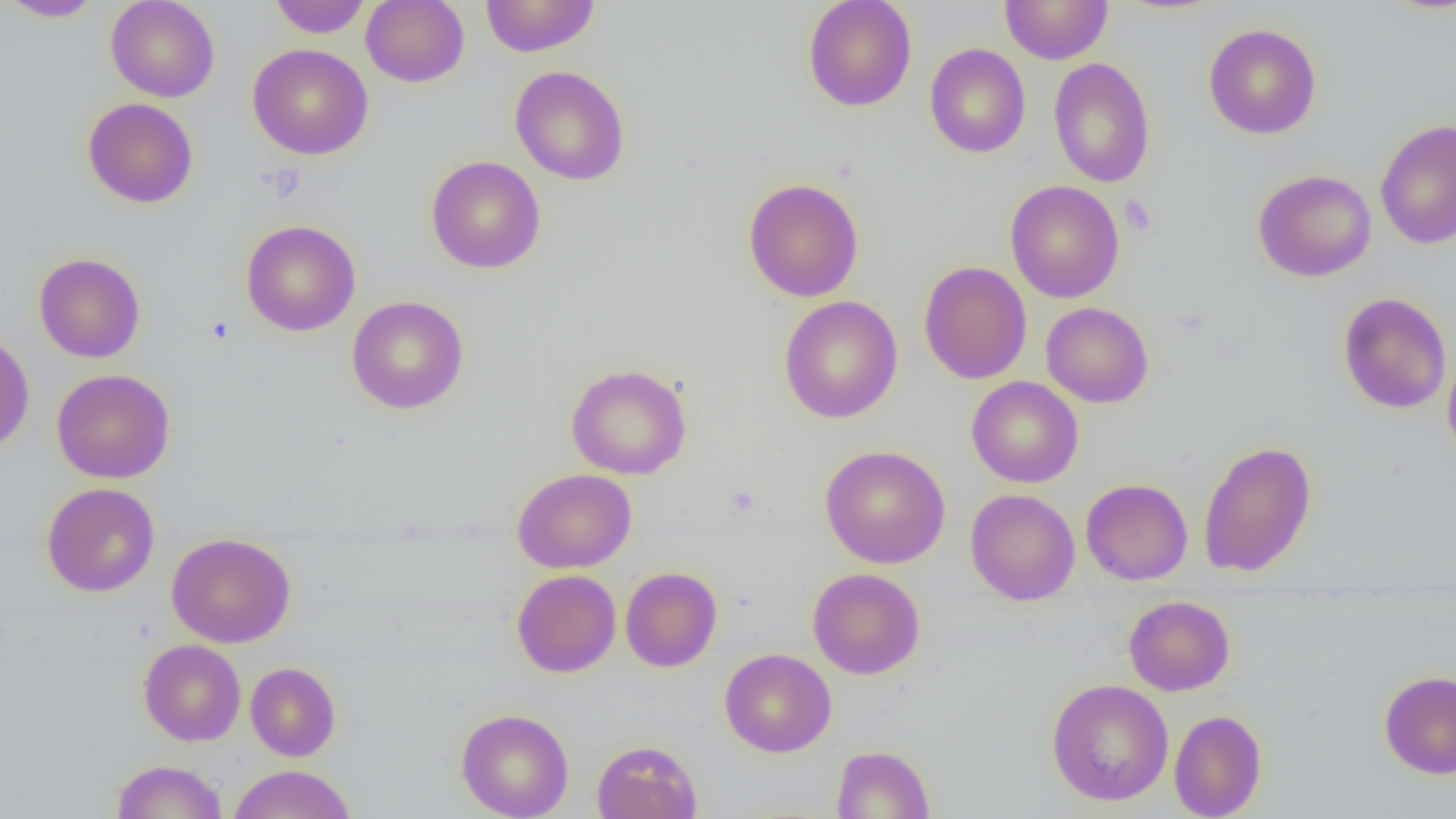

Summary:
  - Coordinate format: approximate bounding boxes as [x1, y1, x2, y2] in pixels
  - Uninfected red blood cell locations: [2, 0, 105, 22], [105, 0, 220, 102], [268, 0, 371, 38], [361, 0, 470, 87], [480, 0, 600, 57], [803, 0, 917, 111], [1000, 0, 1113, 64], [1203, 23, 1322, 139], [247, 43, 373, 160], [925, 43, 1030, 158], [1048, 57, 1156, 188], [510, 65, 630, 185], [83, 98, 198, 208], [1375, 119, 1456, 249], [426, 155, 545, 274], [1252, 169, 1377, 282], [742, 177, 865, 302], [1005, 180, 1124, 303], [241, 220, 361, 336], [33, 252, 146, 363], [918, 261, 1032, 384], [1338, 293, 1452, 413], [347, 295, 469, 414], [779, 296, 903, 423], [1041, 302, 1154, 408], [0, 332, 34, 455], [1442, 352, 1456, 466], [566, 363, 692, 480], [51, 369, 175, 483], [966, 376, 1083, 488], [1198, 440, 1317, 578], [820, 444, 950, 568], [512, 468, 636, 573], [1081, 478, 1193, 585], [41, 482, 160, 597], [965, 489, 1080, 605], [167, 533, 295, 648], [620, 566, 722, 672], [808, 567, 925, 679], [512, 569, 621, 677], [1123, 595, 1235, 696], [138, 639, 246, 746], [719, 648, 836, 757], [245, 662, 341, 761], [1378, 670, 1456, 779], [1046, 678, 1174, 805], [455, 708, 574, 819], [1169, 709, 1266, 818], [591, 739, 703, 819], [831, 744, 935, 819], [111, 759, 228, 818], [228, 764, 355, 818]
  - Platelet locations: [260, 163, 306, 203], [1119, 194, 1156, 235], [206, 316, 235, 344], [725, 485, 760, 516]
  - Slide-level diagnosis: no evidence of blood parasites
  - Magnification: 1000x
  - Preparation: thin blood film
  - Field of view: one of a larger specimen
  - Image size: 1456×819 pixels
  - Modality: optical microscopy